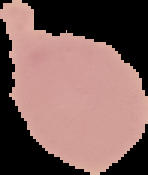

image size = 148×175 pixels
preparation = thin blood smear
malaria status = uninfected
image type = segmented cell region with the area outside set to black